Identify the blood parasite species.
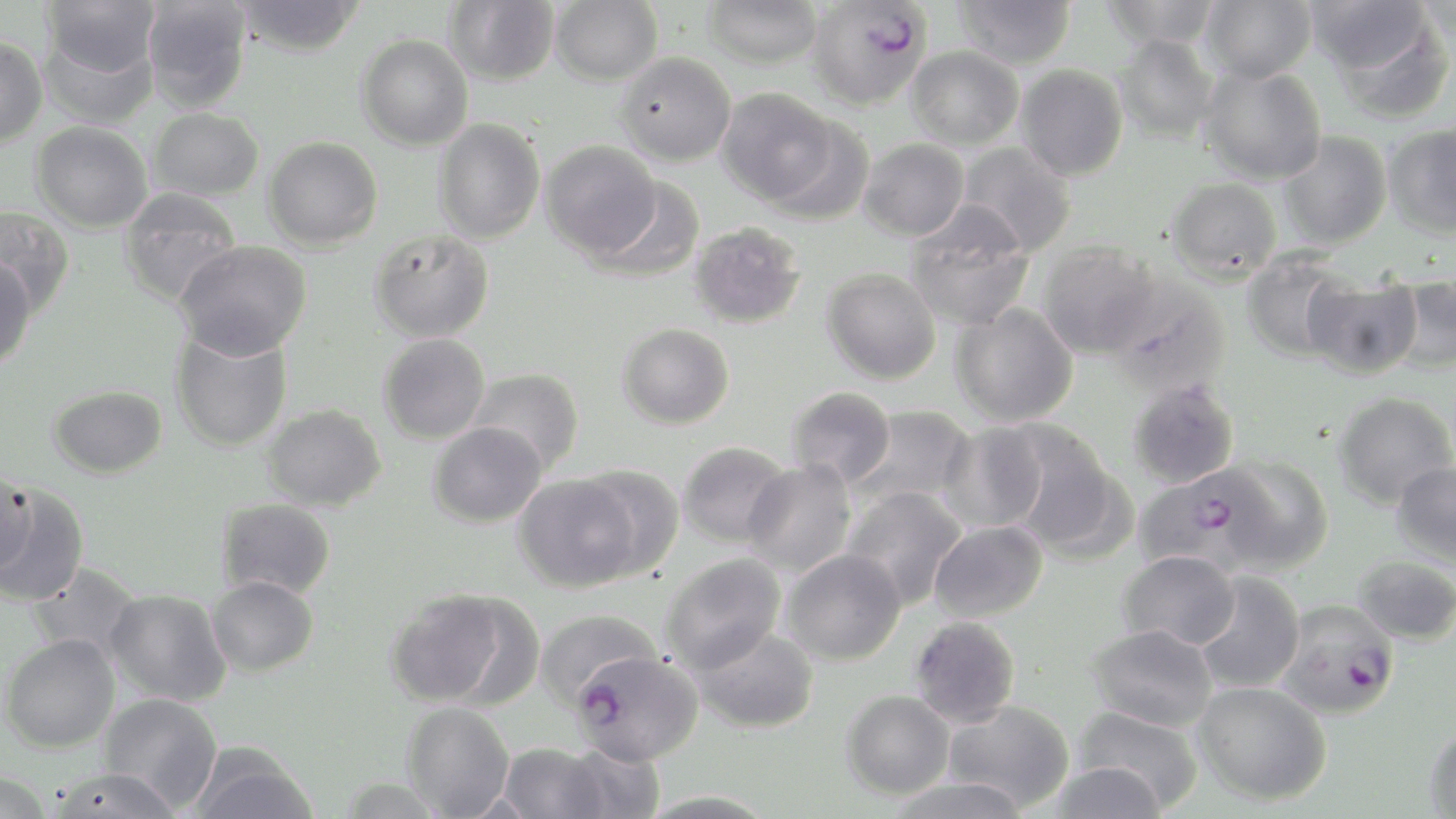
Plasmodium falciparum.

field_of_view: one of a larger specimen
stain: May-Grünwald-Giemsa
uninfected_red_blood_cell_locations: 'approximate bounding boxes as (x1,y1)-(x2,y2) corner pairs in pixels: (42,0)-(162,80), (141,0)-(253,112), (231,0)-(366,57), (445,0)-(560,86), (550,0)-(662,86), (702,0)-(823,69), (953,0)-(1077,69), (1099,0)-(1222,48), (1199,0)-(1316,83), (1304,0)-(1434,77), (1416,0)-(1456,47), (1320,10)-(1453,124), (39,26)-(159,130), (1113,33)-(1221,142), (356,34)-(473,151), (0,36)-(47,147), (905,45)-(1024,150), (615,52)-(736,166), (1015,64)-(1128,180), (1200,64)-(1327,184), (718,88)-(837,205), (148,107)-(264,202), (765,115)-(875,225), (433,117)-(545,244), (31,121)-(153,233), (1382,124)-(1456,239), (1278,131)-(1392,249), (263,136)-(383,250), (858,138)-(969,241), (540,140)-(662,259), (955,143)-(1078,255), (1165,176)-(1282,282), (589,178)-(704,283), (118,187)-(242,305), (904,205)-(1034,331), (0,206)-(76,318), (689,222)-(806,329), (369,230)-(495,343), (174,240)-(312,360), (1038,240)-(1162,359), (1241,249)-(1355,362), (0,256)-(36,371), (822,268)-(941,385), (1303,273)-(1423,379), (1385,274)-(1456,375), (1105,276)-(1232,397), (949,302)-(1078,427), (617,322)-(735,430), (170,327)-(293,453), (378,333)-(490,445), (467,367)-(584,473), (1127,379)-(1240,489), (48,384)-(168,479), (786,386)-(897,489), (1333,392)-(1456,509), (261,404)-(387,511), (851,404)-(975,511), (938,422)-(1048,534), (996,422)-(1124,555), (428,423)-(547,528), (677,441)-(792,549), (1219,455)-(1335,572), (741,460)-(856,577), (1390,461)-(1456,567), (576,464)-(685,579), (0,468)-(38,576), (513,473)-(640,593), (0,482)-(90,608), (841,485)-(968,610), (216,498)-(337,601), (929,520)-(1048,623), (780,549)-(906,666), (1118,550)-(1240,652), (660,553)-(787,673), (1351,555)-(1456,646), (27,563)-(144,663), (1192,571)-(1306,694), (206,576)-(319,677), (105,588)-(231,707), (385,589)-(512,708), (535,609)-(662,710), (909,616)-(1022,728), (1087,623)-(1217,732), (691,625)-(819,733), (1,633)-(121,754), (1191,681)-(1332,806), (841,690)-(955,799), (98,693)-(223,811), (943,700)-(1075,812), (401,701)-(515,817), (1072,704)-(1204,812), (1424,722)-(1456,817), (189,741)-(319,819), (560,741)-(666,819), (498,743)-(608,819), (1045,760)-(1167,819), (44,766)-(184,818), (0,771)-(56,819), (884,775)-(1031,819)'
plasmodium_falciparum_infected_red_blood_cell_locations: 'approximate bounding boxes as (x1,y1)-(x2,y2) corner pairs in pixels: (810,2)-(937,112), (1135,466)-(1273,576), (1274,598)-(1400,720), (572,650)-(701,766)'
image_size: 1456×819 pixels
preparation: thin blood film
magnification: 1000x
modality: optical microscopy